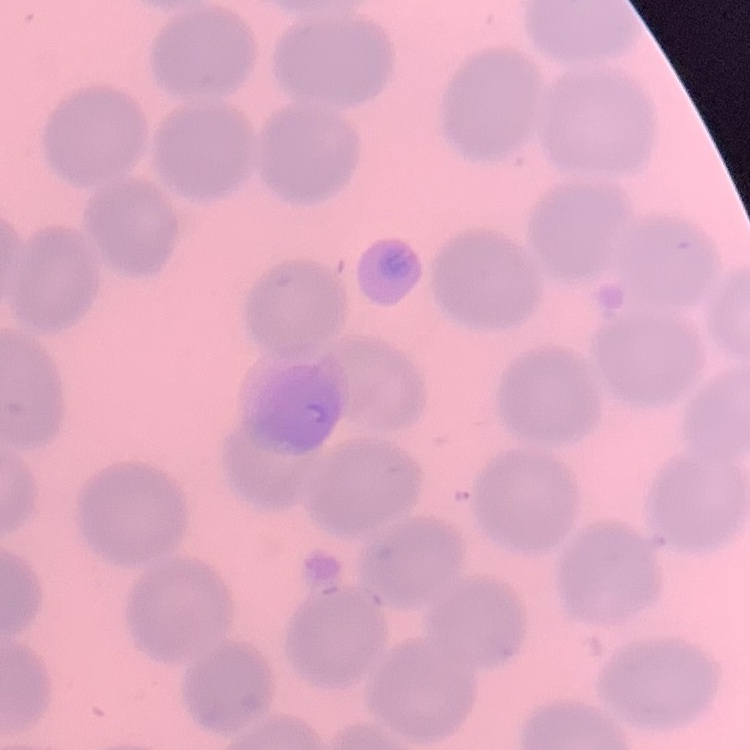 The red blood cells show no rouleaux formation. Stained with either Field's or Giemsa. Thin blood smear. One tile cut from a larger photomicrograph.